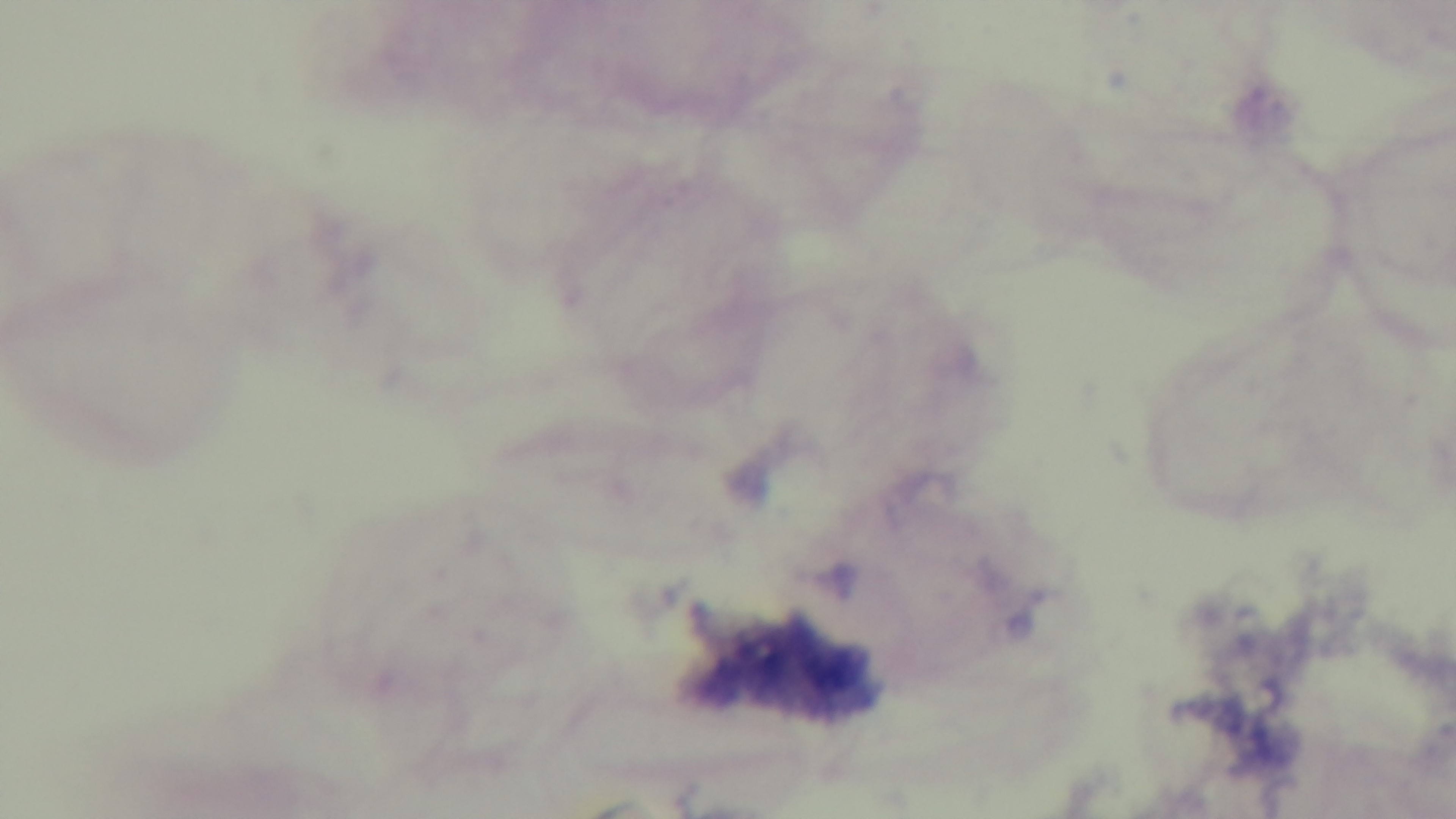
{
  "preparation": "thick",
  "capture": "mounted 4K digital camera",
  "stain": "Giemsa",
  "objective": "100x oil immersion",
  "malaria_status": "uninfected",
  "field_of_view": "single",
  "modality": "light microscopy"
}